Give the extent of all Plasmodium malariae-infected red blood cells.
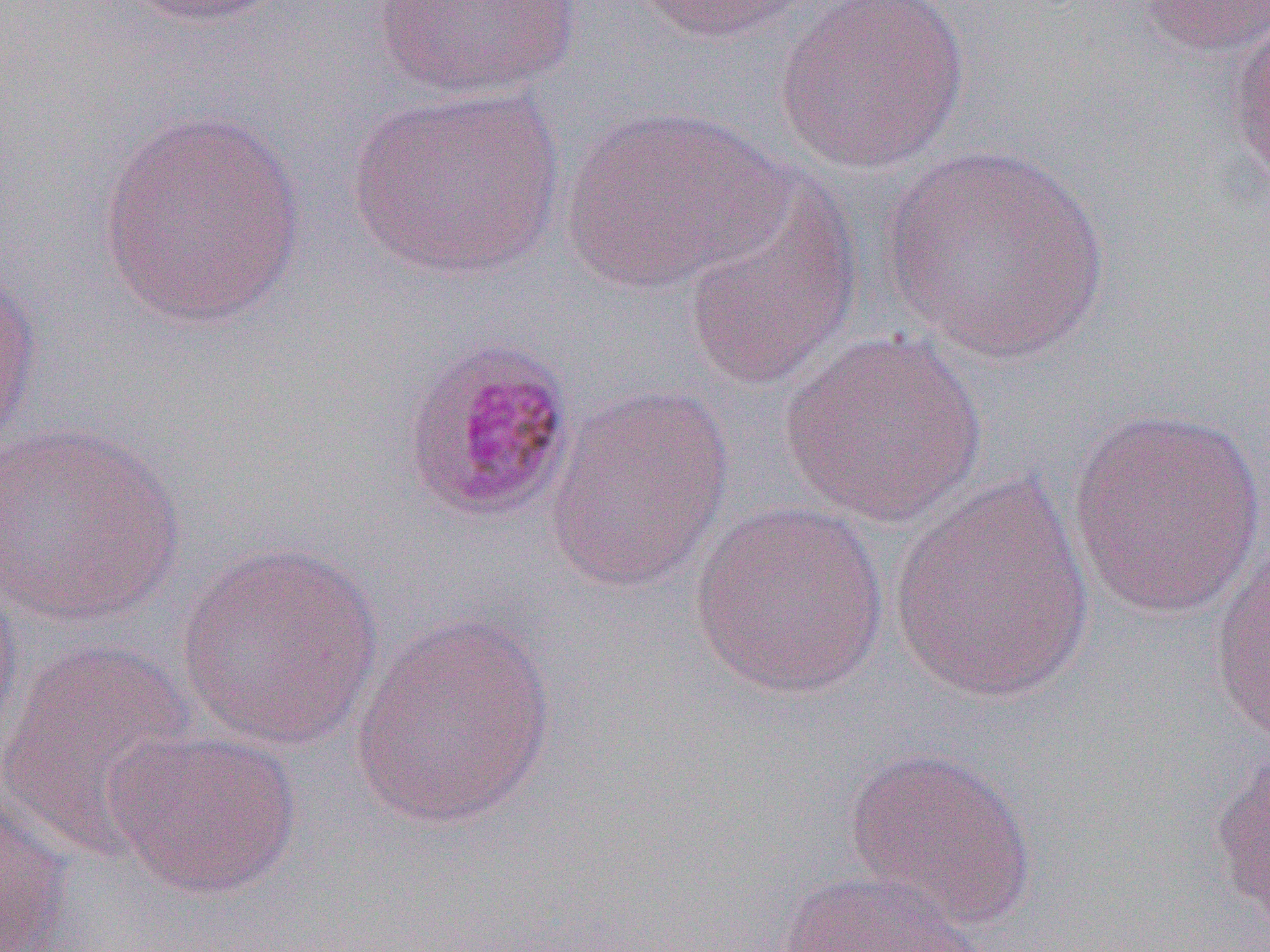
Approximate bounding boxes as (x1, y1, x2, y2) in pixels.
Plasmodium malariae-infected red blood cells: (397, 335, 580, 526).

Summary:
  - Uninfected red blood cell locations: (120, 0, 292, 29), (628, 0, 824, 44), (770, 0, 969, 174), (1133, 0, 1270, 59), (372, 1, 585, 102), (1227, 14, 1270, 187), (345, 86, 566, 282), (560, 105, 789, 295), (96, 110, 308, 327), (882, 144, 1109, 363), (679, 174, 865, 392), (0, 266, 42, 457), (779, 330, 988, 526), (545, 385, 735, 594), (1067, 405, 1269, 623), (1, 420, 187, 628), (890, 471, 1097, 705), (688, 500, 892, 699), (1207, 529, 1270, 750), (174, 541, 385, 750), (0, 570, 23, 763), (349, 611, 560, 830), (0, 635, 198, 860), (104, 727, 303, 901), (1207, 740, 1270, 935), (843, 745, 1037, 925), (0, 790, 72, 952), (775, 869, 991, 952)
  - Slide-level diagnosis: Plasmodium malariae
  - Image size: 1270×952 pixels
  - Preparation: thin blood film
  - Modality: light microscopy
  - Field of view: single
  - Magnification: 1000x